Draw a bounding box around every leukocyte (white blood cell).
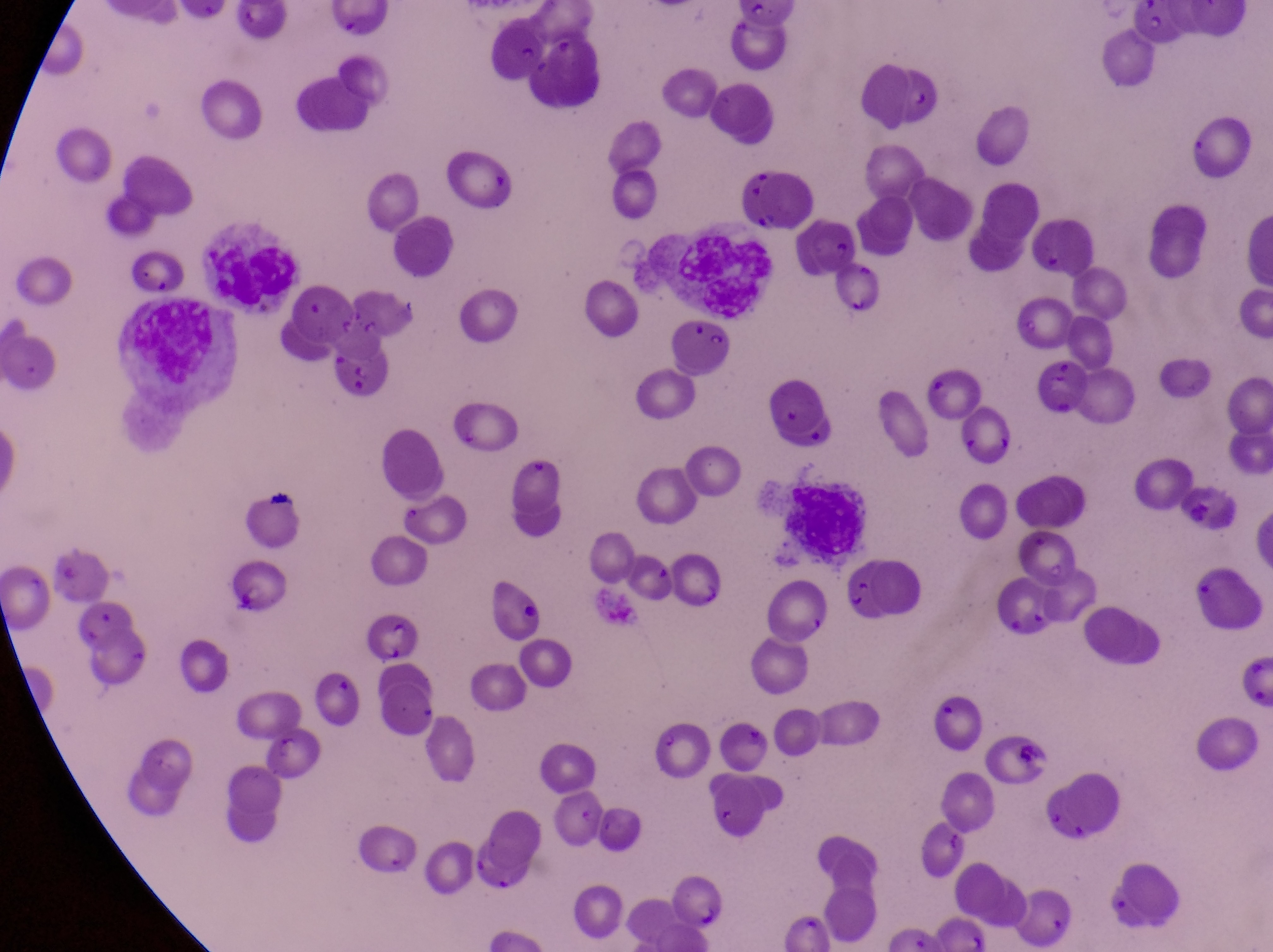
Approximate bounding boxes as left top right bottom in pixels.
Leukocytes: 677 230 767 320; 194 232 304 309; 132 305 227 385; 781 477 874 563.

{
  "magnification": "1000x",
  "parasitised_red_blood_cell_locations": "approximate bounding boxes as left top right bottom in pixels: 803 217 856 272; 369 609 419 667",
  "image_size": "1273×952 pixels",
  "artifact_platelet_like_body_stain_precipitate_or_debris_locations": "approximate bounding boxes as left top right bottom in pixels: 475 155 512 194; 1001 722 1043 772",
  "capture": "smartphone photograph through the eyepiece of an Olympus CX-23 microscope",
  "preparation": "thin blood smear",
  "country": "Uganda",
  "field_of_view": "single"
}